Report the malaria status of this cell.
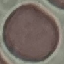

It is uninfected.

Summary:
  - Capture: smartphone through the microscope eyepiece
  - Stain: Giemsa
  - Preparation: thin blood film
  - Image type: cell patch, automatically extracted from a larger field of view and resized to 64 × 64 pixels